Identify the parasite.
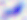

Toxoplasma gondii.

Summary:
  - Magnification: 400x
  - Modality: photomicrograph